Classify this cell by malaria status.
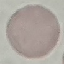

It is uninfected.

Thin blood film. Acquired by smartphone through the microscope eyepiece. Automatically extracted cell patch, resized to 64 × 64 pixels. Giemsa-stained preparation.